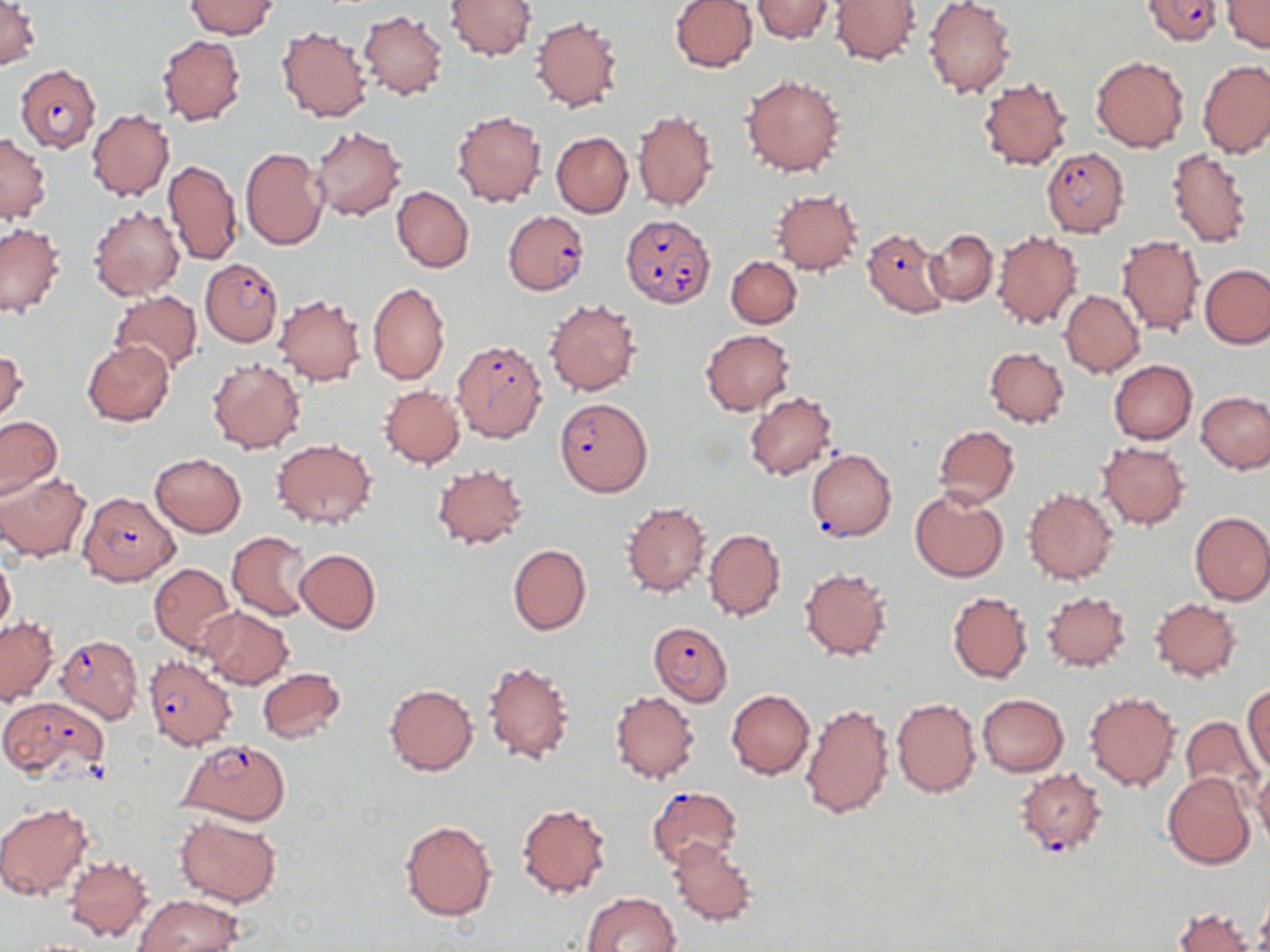
Summary:
  - Coordinate format: approximate bounding boxes as [x1, y1, x2, y2] in pixels
  - Uninfected red blood cell locations: [185, 0, 277, 39], [445, 0, 537, 61], [670, 0, 757, 72], [752, 0, 833, 43], [828, 0, 922, 66], [922, 0, 1017, 98], [1222, 0, 1269, 52], [0, 1, 40, 70], [357, 8, 449, 100], [531, 16, 625, 112], [277, 25, 372, 122], [157, 34, 246, 126], [1091, 55, 1188, 153], [1198, 58, 1270, 157], [1182, 61, 1261, 243], [740, 73, 846, 176], [976, 75, 1074, 171], [87, 109, 174, 201], [632, 109, 719, 213], [452, 110, 547, 207], [309, 127, 406, 221], [551, 131, 632, 218], [1, 132, 50, 224], [241, 146, 327, 250], [1165, 147, 1254, 248], [163, 158, 244, 265], [392, 185, 474, 271], [770, 188, 863, 275], [88, 206, 185, 300], [0, 223, 65, 319], [925, 228, 997, 305], [991, 230, 1083, 331], [1116, 235, 1204, 337], [726, 255, 801, 328], [1200, 264, 1270, 349], [368, 281, 449, 385], [1059, 290, 1144, 377], [108, 291, 202, 375], [274, 294, 367, 386], [544, 298, 642, 396], [700, 329, 794, 416], [82, 339, 174, 426], [984, 346, 1069, 428], [0, 348, 27, 427], [207, 357, 306, 454], [1108, 360, 1197, 443], [378, 385, 465, 468], [743, 392, 837, 481], [1196, 392, 1270, 474], [0, 416, 63, 498], [933, 424, 1019, 507], [270, 437, 377, 531], [1097, 440, 1190, 531], [150, 453, 246, 536], [431, 464, 530, 550], [0, 472, 89, 562], [1024, 487, 1119, 584], [910, 488, 1008, 582], [621, 501, 711, 598], [1189, 511, 1270, 606], [703, 528, 786, 621], [227, 531, 313, 621], [508, 544, 591, 635], [295, 548, 380, 635], [0, 555, 15, 637], [150, 562, 237, 652], [800, 565, 895, 663], [1041, 590, 1131, 672], [947, 591, 1032, 684], [1150, 598, 1241, 680], [199, 607, 294, 689], [0, 616, 57, 705], [480, 658, 576, 767], [256, 667, 346, 743], [384, 684, 478, 775], [1242, 686, 1270, 776], [726, 689, 814, 780], [1084, 689, 1181, 792], [609, 691, 700, 783], [976, 693, 1069, 777], [892, 697, 980, 798], [800, 701, 893, 821], [1179, 715, 1262, 803], [1253, 767, 1270, 850], [1163, 772, 1255, 869], [516, 802, 613, 899], [0, 804, 93, 900], [173, 812, 284, 908], [400, 818, 498, 922], [666, 839, 760, 927], [65, 855, 152, 942], [1256, 885, 1270, 952], [580, 891, 681, 952], [133, 894, 239, 952], [1174, 907, 1254, 952]
  - Plasmodium falciparum-infected red blood cell locations: [1140, 0, 1226, 45], [15, 64, 101, 152], [1040, 147, 1129, 237], [502, 211, 589, 294], [620, 215, 715, 306], [862, 228, 949, 318], [200, 259, 282, 346], [451, 338, 548, 443], [553, 397, 652, 496], [806, 449, 896, 541], [75, 493, 179, 586], [648, 622, 732, 704], [55, 634, 143, 723], [143, 655, 236, 751], [0, 696, 109, 779], [177, 739, 291, 826], [1015, 767, 1107, 857], [647, 785, 743, 869]
  - Slide-level diagnosis: Plasmodium falciparum
  - Field of view: single
  - Magnification: 1000x
  - Stain: May-Grünwald-Giemsa
  - Preparation: thin blood film
  - Modality: light microscopy
  - Image size: 1270×952 pixels